Comment on the morphology of the erythrocytes.
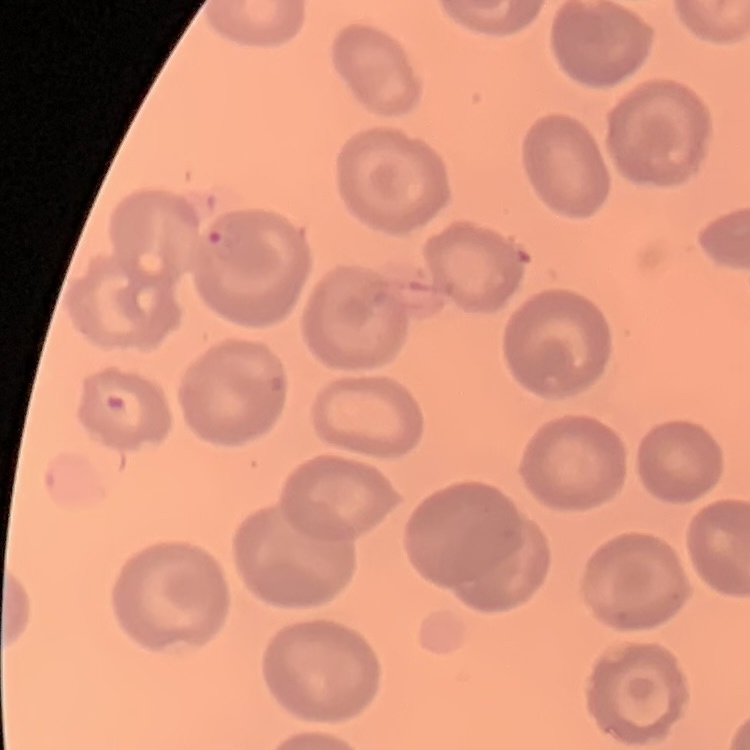

They show no rouleaux formation.

Stained with either Field's or Giemsa. Square crop of a larger photomicrograph. Thin blood film.